Identify the parasite.
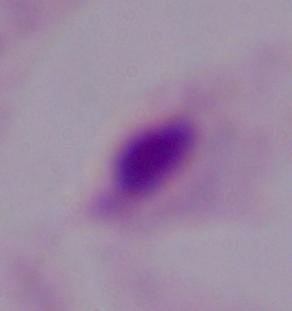

A trichomonad.

{
  "magnification": "1000x",
  "modality": "photomicrograph"
}